Name the parasite shown.
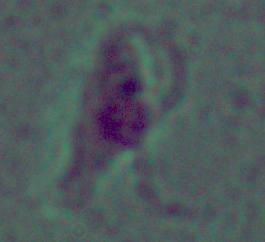

Leishmania.

Micrograph. 1000x magnification.